Assess this cell for malaria.
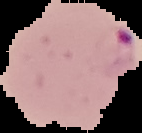
Parasitized.

image type = segmented cell region with the area outside set to black
image size = 142×133 pixels
preparation = thin blood film